Report the malaria status of this cell.
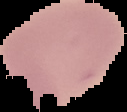

Uninfected.

From a thin blood film. Image is 127×112 pixels. The area outside the segmented cell region is set to black.